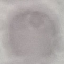

Summary:
  - Result: no malaria parasites detected
  - Preparation: thin smear
  - Image type: cell patch, automatically extracted from a larger field of view and resized to 64 × 64 pixels
  - Stain: Giemsa
  - Capture: smartphone camera at the microscope eyepiece